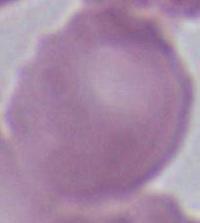

Captured at 1000x magnification. Micrograph. A red blood cell is seen.